Assess this cell for malaria.
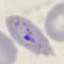
It is parasitized.

Summary:
  - Image type: automatically extracted cell patch, resized to 64 × 64 pixels
  - Stain: Giemsa
  - Preparation: thin blood smear
  - Capture: smartphone through the microscope eyepiece